Classify this cell by malaria status.
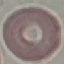

Uninfected.

Summary:
  - Preparation: thin smear
  - Capture: smartphone through the microscope eyepiece
  - Image type: automatically extracted cell patch, resized to 64 × 64 pixels
  - Stain: Giemsa